Assess the morphology of the red blood cells.
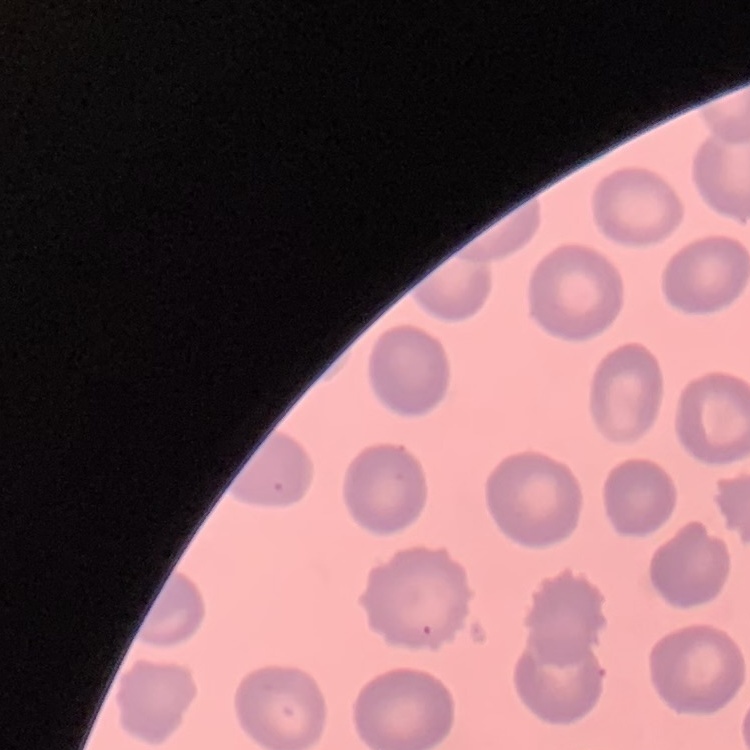

They show no rouleaux formation.

stain = Field's or Giemsa
image type = square crop of a larger photomicrograph
preparation = thin blood film